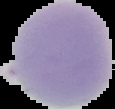

{
  "preparation": "thin blood film",
  "malaria_status": "uninfected",
  "image_size": "115×109 pixels",
  "image_type": "segmented cell region with the area outside set to black"
}